Report the malaria status of this cell.
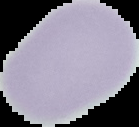

Uninfected.

preparation = thin blood film
image size = 139×127 pixels
image type = cell region segmented out of the field of view; surrounding area masked to black